Identify the cell.
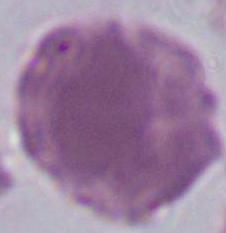
An erythrocyte.

modality = micrograph
magnification = 1000x